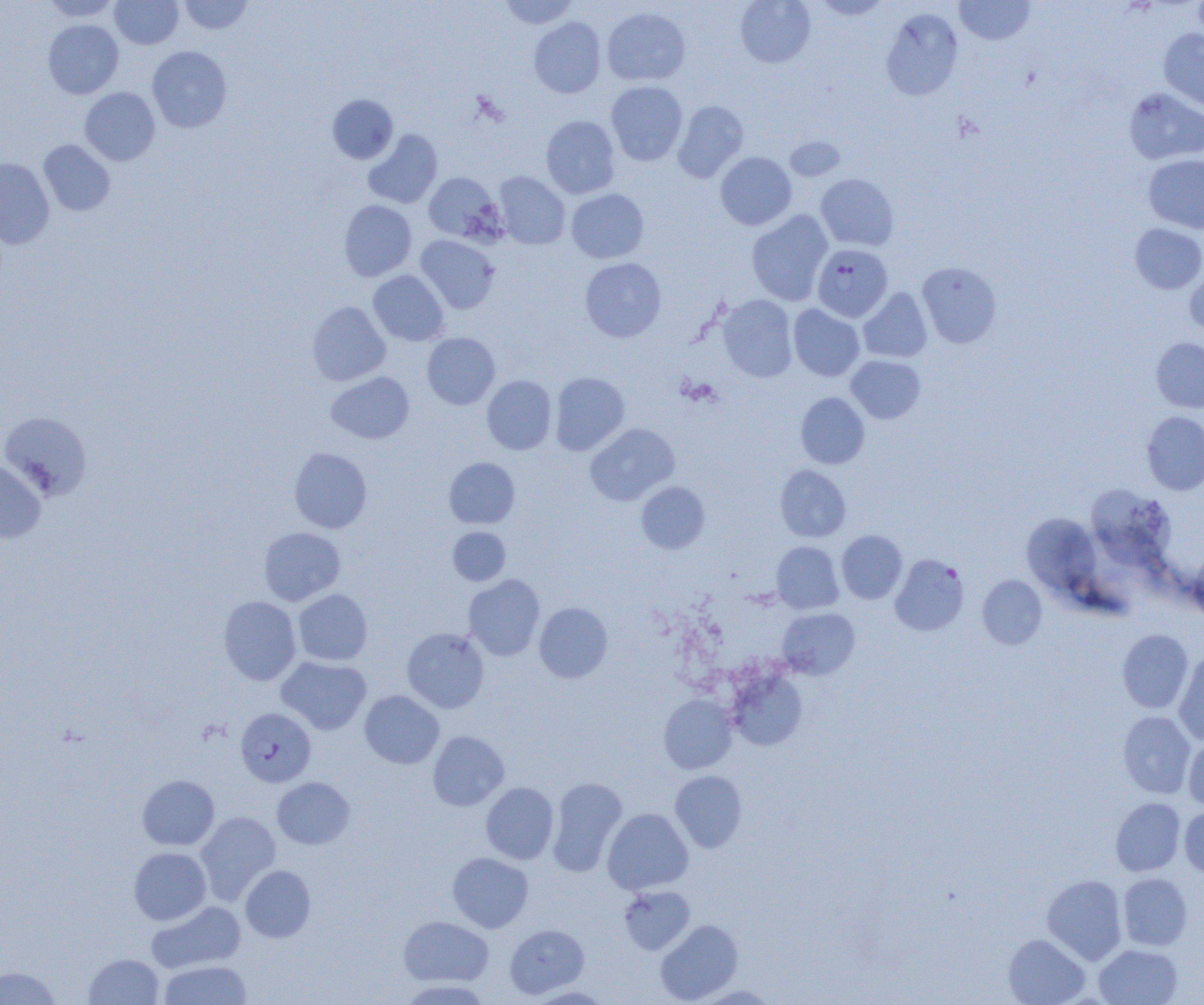

slide_level_diagnosis: Plasmodium falciparum
modality: light microscopy
preparation: thin blood film
uninfected_red_blood_cell_locations: 'approximate bounding boxes as (x1, y1, x2, y2) in pixels: (42, 0, 121, 21), (110, 0, 183, 49), (179, 0, 253, 34), (499, 0, 578, 29), (735, 0, 816, 68), (812, 0, 891, 20), (955, 0, 1034, 45), (1193, 0, 1204, 47), (602, 7, 690, 86), (881, 8, 963, 100), (529, 17, 606, 98), (43, 19, 123, 99), (1159, 29, 1204, 113), (147, 46, 232, 133), (606, 81, 687, 165), (80, 87, 160, 165), (1124, 87, 1204, 165), (327, 94, 398, 164), (672, 100, 749, 182), (541, 115, 621, 198), (363, 129, 442, 209), (784, 136, 846, 181), (38, 140, 115, 216), (715, 152, 796, 230), (1143, 154, 1204, 233), (0, 158, 55, 249), (423, 172, 504, 243), (494, 172, 570, 249), (816, 173, 899, 251), (566, 189, 649, 263), (339, 200, 416, 281), (746, 210, 833, 306), (1130, 224, 1204, 294), (415, 235, 499, 314), (580, 258, 666, 342), (918, 262, 1001, 348), (1185, 267, 1204, 335), (368, 270, 449, 346), (858, 288, 932, 363), (717, 295, 797, 382), (307, 301, 390, 385), (788, 304, 864, 381), (422, 333, 500, 409), (1151, 337, 1204, 413), (846, 355, 924, 424), (326, 372, 414, 444), (550, 372, 629, 455), (482, 375, 556, 455), (796, 392, 870, 469), (1, 411, 93, 498), (1142, 411, 1204, 495), (585, 423, 679, 505), (289, 447, 372, 533), (444, 457, 520, 528), (0, 459, 46, 544), (775, 465, 851, 542), (636, 481, 710, 554), (1090, 485, 1172, 570), (1021, 513, 1100, 596), (259, 527, 345, 606), (447, 527, 510, 585), (836, 530, 907, 604), (771, 541, 844, 613), (1189, 550, 1204, 620), (890, 554, 969, 635), (463, 574, 545, 661), (978, 575, 1047, 649), (293, 589, 373, 666), (218, 596, 301, 685), (534, 602, 612, 683), (777, 607, 860, 679), (402, 628, 488, 713), (1117, 629, 1193, 713), (1174, 652, 1204, 745), (276, 656, 371, 735), (727, 670, 807, 750), (360, 690, 444, 769), (659, 694, 737, 774), (1118, 711, 1195, 798), (428, 731, 509, 811), (1184, 739, 1204, 810), (670, 771, 747, 852), (137, 775, 219, 850), (272, 777, 355, 849), (547, 777, 627, 876), (481, 782, 559, 864), (1111, 798, 1185, 876), (1179, 807, 1204, 878), (602, 808, 693, 895), (195, 811, 280, 905), (129, 847, 211, 925), (448, 852, 533, 932), (241, 865, 315, 942), (1118, 873, 1192, 951), (1042, 875, 1127, 964), (619, 885, 695, 955), (147, 901, 246, 973), (399, 916, 493, 986), (655, 920, 743, 1004), (505, 924, 589, 999), (1003, 934, 1089, 1005), (1094, 944, 1182, 1005), (84, 953, 164, 1005), (158, 959, 252, 1004), (0, 967, 60, 1005), (400, 979, 491, 1004), (693, 985, 780, 1004), (526, 986, 611, 1004)'
image_size: 1204×1005 pixels
plasmodium_falciparum_infected_red_blood_cell_locations: 'approximate bounding boxes as (x1, y1, x2, y2) in pixels: (812, 244, 893, 321), (235, 707, 316, 786)'
field_of_view: one of a larger specimen
magnification: 1000x